Outline every leukocyte.
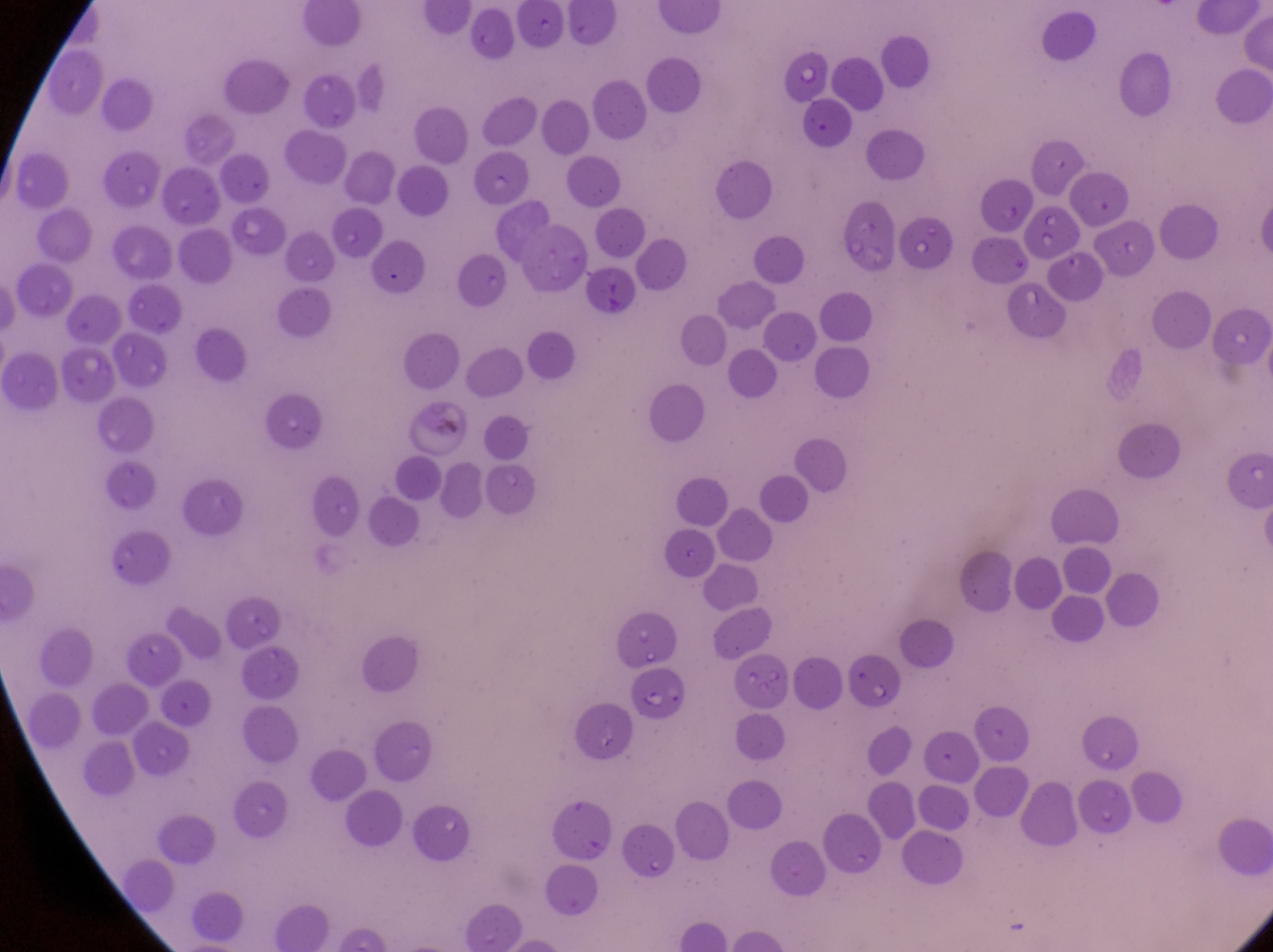

No leukocytes observed.

country = Uganda
artifact (platelet-like body, stain precipitate, or debris) locations = approximate bounding boxes as {left, top, right, bottom} in pixels: {229, 207, 289, 259}, {430, 415, 462, 442}
field of view = single
capture = smartphone photograph through the eyepiece of an Olympus CX-23 microscope
parasitised red blood cell locations = approximate bounding boxes as {left, top, right, bottom} in pixels: {472, 152, 530, 207}, {1026, 202, 1079, 260}, {846, 654, 903, 707}, {627, 667, 690, 724}
magnification = 1000x
preparation = thin blood smear
image size = 1273×952 pixels